Locate every blood parasite and identify its species.
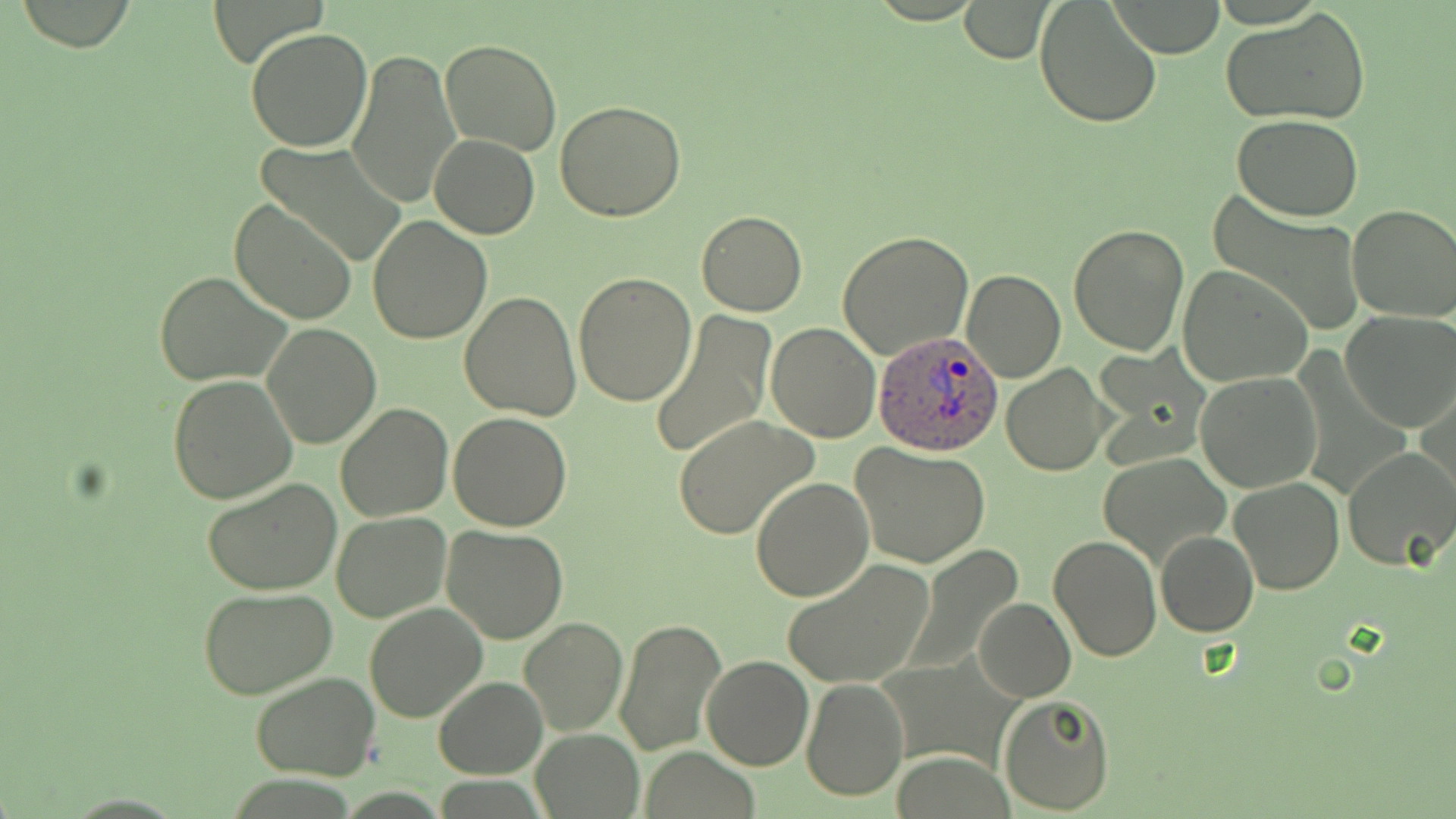

Approximate bounding boxes as named x1/y1/x2/y2 corners in pixels.
Plasmodium ovale-infected red blood cells: (x1=871, y1=331, x2=1003, y2=455).
No Plasmodium falciparum, Plasmodium malariae, Plasmodium vivax, Babesia divergens, or Trypanosoma brucei observed.

Summary:
  - Uninfected red blood cell locations: (x1=1034, y1=0, x2=1163, y2=127), (x1=961, y1=1, x2=1051, y2=62), (x1=1111, y1=2, x2=1225, y2=59), (x1=1221, y1=9, x2=1373, y2=126), (x1=245, y1=28, x2=374, y2=152), (x1=440, y1=38, x2=562, y2=156), (x1=345, y1=48, x2=461, y2=208), (x1=555, y1=100, x2=688, y2=222), (x1=1232, y1=114, x2=1364, y2=220), (x1=430, y1=134, x2=539, y2=238), (x1=255, y1=142, x2=407, y2=261), (x1=1207, y1=191, x2=1366, y2=339), (x1=229, y1=197, x2=358, y2=325), (x1=1346, y1=204, x2=1456, y2=322), (x1=695, y1=211, x2=807, y2=317), (x1=368, y1=215, x2=492, y2=342), (x1=1068, y1=223, x2=1190, y2=357), (x1=837, y1=232, x2=973, y2=358), (x1=1178, y1=264, x2=1312, y2=386), (x1=961, y1=269, x2=1066, y2=382), (x1=156, y1=272, x2=292, y2=387), (x1=574, y1=272, x2=696, y2=406), (x1=460, y1=291, x2=581, y2=422), (x1=648, y1=308, x2=776, y2=463), (x1=1341, y1=311, x2=1456, y2=431), (x1=261, y1=322, x2=381, y2=449), (x1=766, y1=323, x2=882, y2=441), (x1=1090, y1=345, x2=1210, y2=463), (x1=1002, y1=364, x2=1111, y2=476), (x1=1196, y1=371, x2=1324, y2=494), (x1=167, y1=375, x2=297, y2=504), (x1=1417, y1=388, x2=1454, y2=516), (x1=336, y1=401, x2=454, y2=520), (x1=448, y1=413, x2=573, y2=531), (x1=672, y1=415, x2=817, y2=539), (x1=850, y1=443, x2=993, y2=570), (x1=1342, y1=447, x2=1456, y2=571), (x1=1098, y1=456, x2=1228, y2=568), (x1=1228, y1=475, x2=1344, y2=594), (x1=203, y1=477, x2=342, y2=596), (x1=751, y1=478, x2=873, y2=602), (x1=332, y1=512, x2=451, y2=622), (x1=441, y1=525, x2=567, y2=644), (x1=1155, y1=531, x2=1257, y2=637), (x1=1047, y1=533, x2=1161, y2=663), (x1=903, y1=546, x2=1026, y2=673), (x1=780, y1=558, x2=935, y2=689), (x1=197, y1=586, x2=337, y2=699), (x1=974, y1=598, x2=1075, y2=701), (x1=364, y1=603, x2=487, y2=723), (x1=520, y1=617, x2=628, y2=735), (x1=615, y1=619, x2=727, y2=755), (x1=701, y1=654, x2=814, y2=769), (x1=249, y1=672, x2=381, y2=780), (x1=433, y1=677, x2=546, y2=778), (x1=802, y1=679, x2=908, y2=803), (x1=997, y1=693, x2=1115, y2=815), (x1=531, y1=728, x2=644, y2=817), (x1=641, y1=747, x2=760, y2=819)
  - Slide-level diagnosis: Plasmodium ovale
  - Field of view: one of a larger specimen
  - Magnification: 1000x
  - Modality: optical microscopy
  - Preparation: thin blood film
  - Image size: 1456×819 pixels
  - Stain: May-Grünwald-Giemsa